Identify the preparation type.
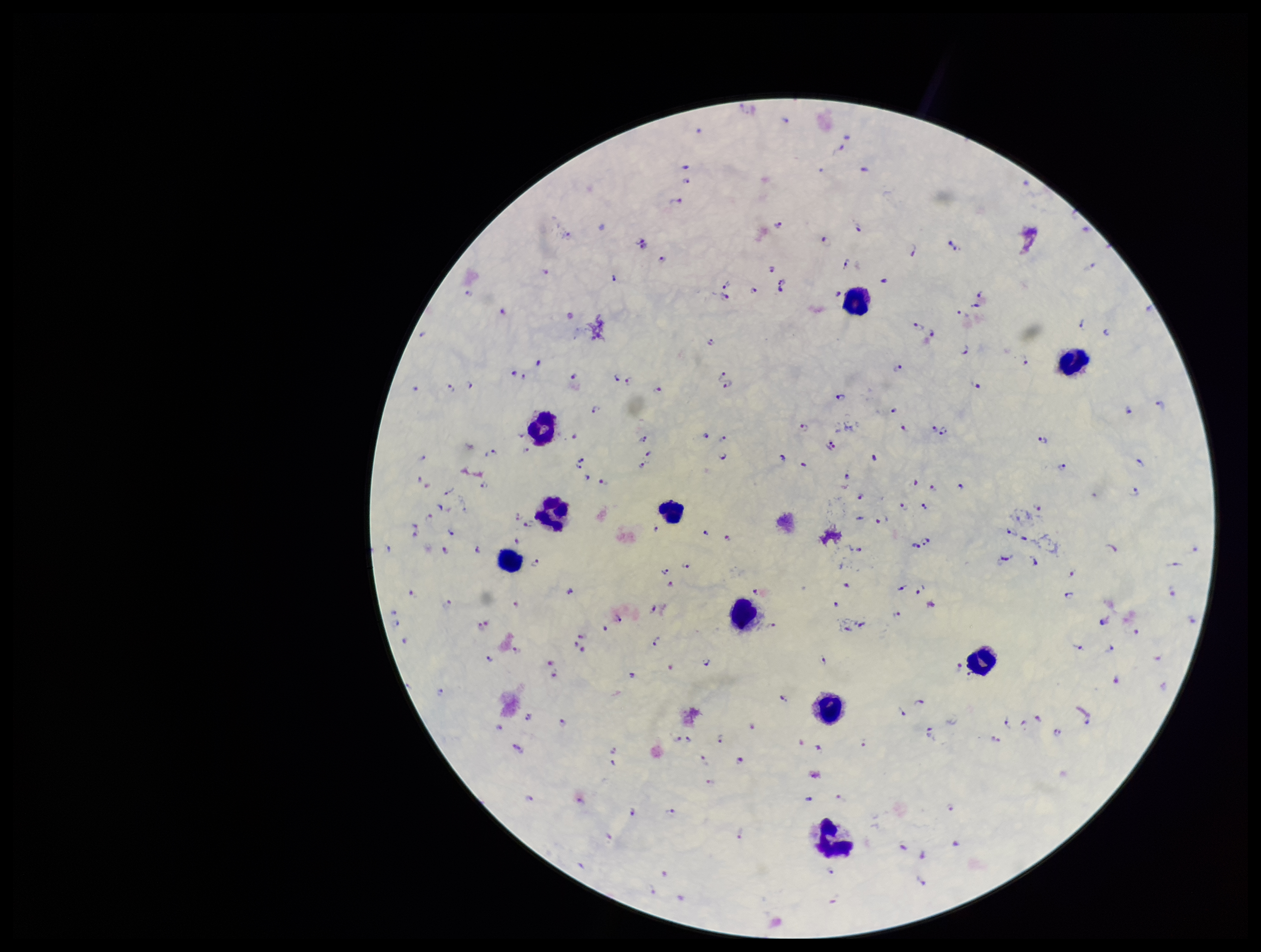

A thick smear.

Giemsa stain. Smartphone photograph taken through the eyepiece of a microscope. One field from this slide. Parasite count: 182. Leukocyte count: 10. Species reported for this patient: Plasmodium falciparum. Image is 1261×952 pixels. Plasmodium parasites: identified. Patient malaria status: positive.